Name the blood parasite species.
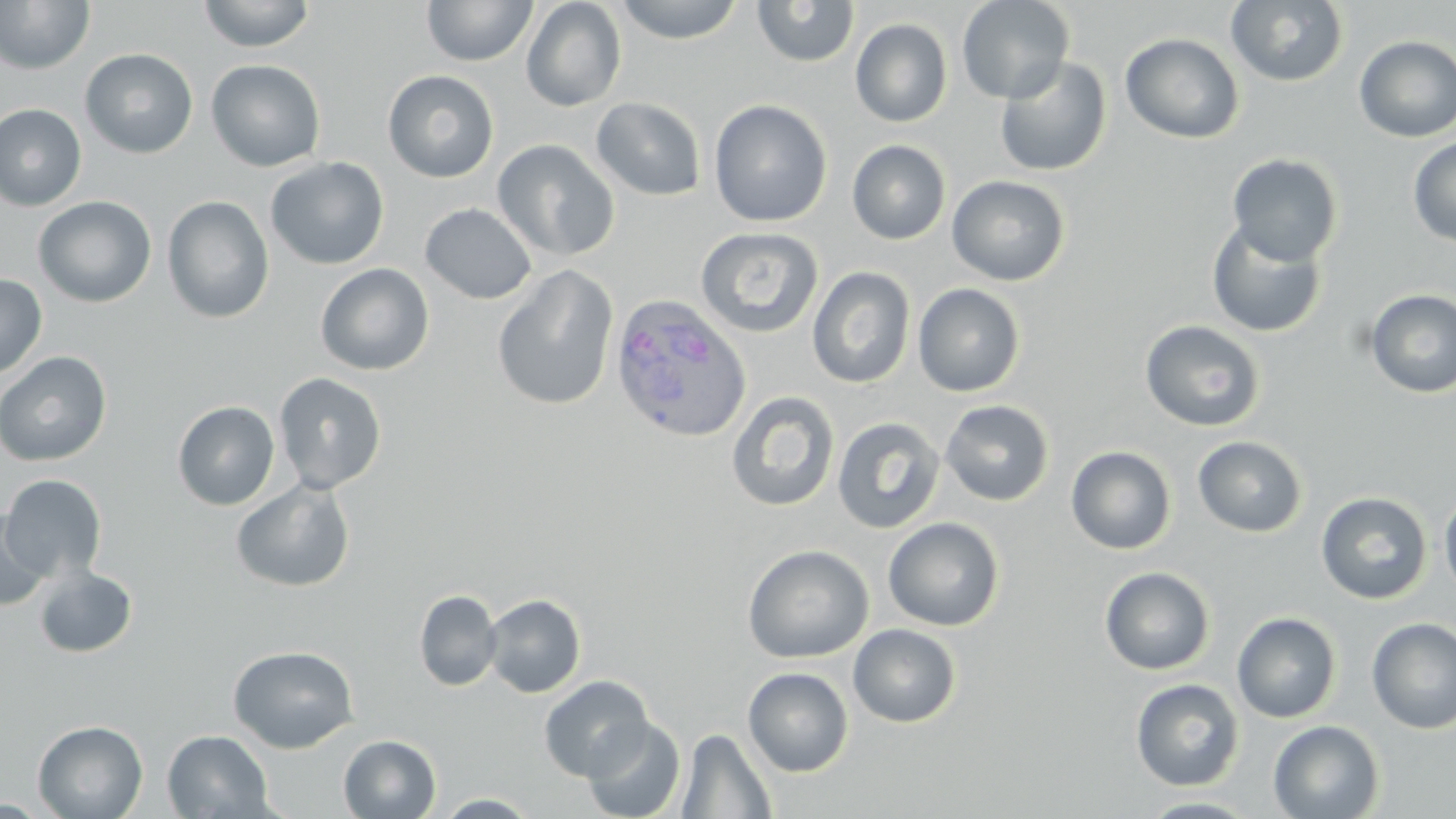
Plasmodium ovale.

Summary:
  - Coordinate format: approximate bounding boxes as [x1, y1, x2, y2] in pixels
  - Uninfected red blood cell locations: [0, 0, 95, 75], [197, 0, 316, 52], [520, 0, 626, 112], [613, 0, 746, 44], [957, 0, 1075, 104], [1226, 0, 1349, 87], [421, 1, 538, 67], [751, 1, 860, 67], [850, 18, 952, 128], [1120, 32, 1244, 144], [1354, 35, 1456, 142], [80, 48, 198, 158], [994, 56, 1112, 177], [206, 59, 326, 172], [382, 69, 500, 183], [591, 97, 706, 201], [708, 99, 833, 227], [0, 103, 87, 211], [1407, 136, 1456, 247], [492, 139, 620, 262], [847, 140, 951, 245], [1227, 153, 1343, 266], [265, 157, 389, 269], [947, 175, 1070, 286], [161, 195, 275, 324], [33, 196, 157, 308], [419, 203, 538, 304], [1205, 219, 1327, 339], [695, 227, 824, 338], [314, 263, 434, 376], [492, 265, 619, 412], [807, 266, 916, 388], [0, 273, 47, 380], [913, 283, 1025, 397], [1364, 289, 1456, 398], [1140, 319, 1266, 432], [0, 351, 112, 466], [273, 372, 387, 495], [726, 390, 840, 512], [172, 400, 280, 510], [940, 400, 1055, 506], [832, 416, 945, 535], [1192, 436, 1307, 538], [1066, 446, 1176, 555], [1, 474, 107, 583], [231, 479, 356, 593], [1439, 490, 1456, 600], [1315, 492, 1433, 605], [0, 508, 52, 611], [883, 517, 1005, 631], [742, 544, 874, 663], [33, 566, 137, 658], [1100, 566, 1215, 675], [414, 589, 502, 692], [482, 593, 586, 698], [1232, 612, 1342, 723], [1366, 618, 1456, 734], [848, 624, 961, 728], [228, 644, 359, 753], [743, 667, 854, 777], [538, 675, 654, 782], [1130, 678, 1244, 791], [581, 717, 686, 819], [32, 720, 148, 819], [1268, 720, 1384, 819], [677, 728, 776, 818], [162, 730, 275, 818], [338, 734, 441, 819], [433, 793, 539, 817], [1137, 796, 1264, 818]
  - Plasmodium ovale-infected red blood cell locations: [607, 293, 751, 444]
  - Field of view: one of a larger specimen
  - Preparation: thin blood film
  - Modality: optical microscopy
  - Magnification: 1000x
  - Stain: May-Grünwald-Giemsa
  - Image size: 1456×819 pixels